Classify this cell by malaria status.
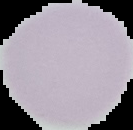
It is uninfected.

image type = segmented cell region on a black background
image size = 133×130 pixels
preparation = thin blood film